Report the malaria status of this cell.
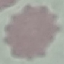
It is uninfected.

Automatically extracted cell patch, resized to 64 × 64 pixels. Giemsa stain. Acquired by smartphone through the microscope eyepiece. Thin blood smear.